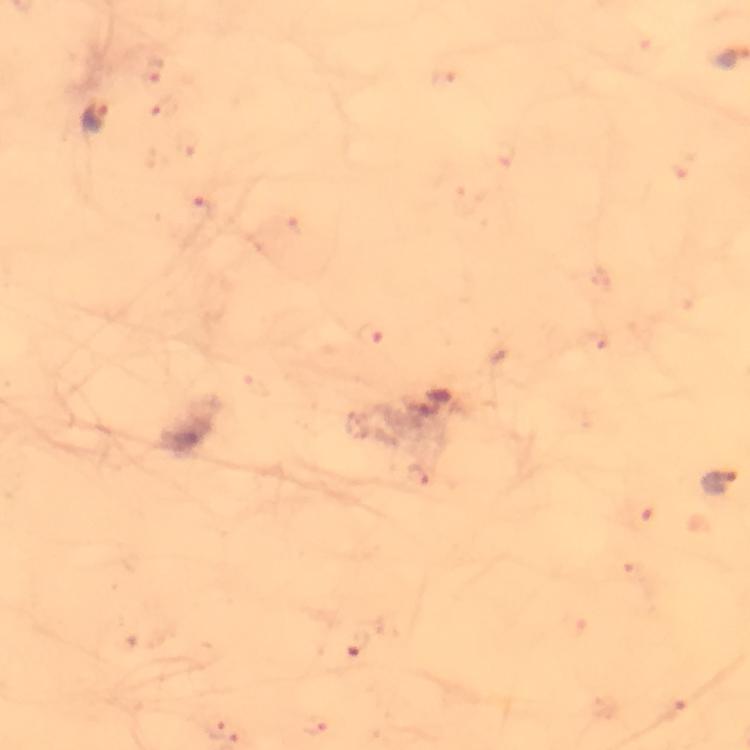

Approximate object centers, in pixels from the top-left corner. Malaria parasite locations: (x=96, y=119), (x=718, y=482). 100x magnification. From a diagnostic examination for malaria. Thick smear. A crop from one field of view. Image is 750×750 pixels. Giemsa stain. Photographed with a smartphone mounted on the microscope. Immersion oil applied.